Report the malaria status of this cell.
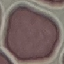
Uninfected.

Summary:
  - Capture: smartphone through the microscope eyepiece
  - Stain: Giemsa
  - Preparation: thin blood film
  - Image type: cell patch, automatically extracted from a larger field of view and resized to 64 × 64 pixels